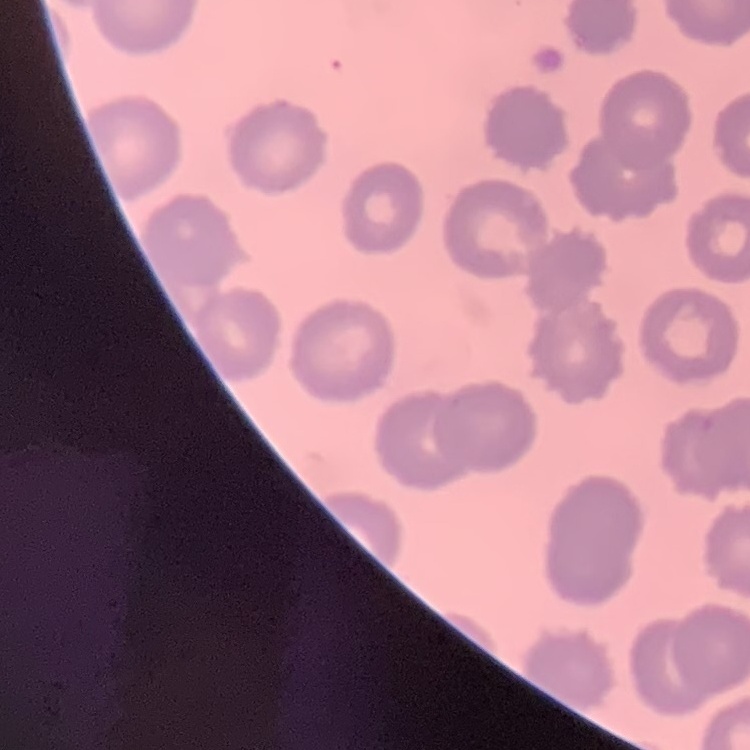
red blood cell morphology = no rouleaux formation
stain = Field's or Giemsa
preparation = thin blood smear
image type = one tile cut from a larger photomicrograph